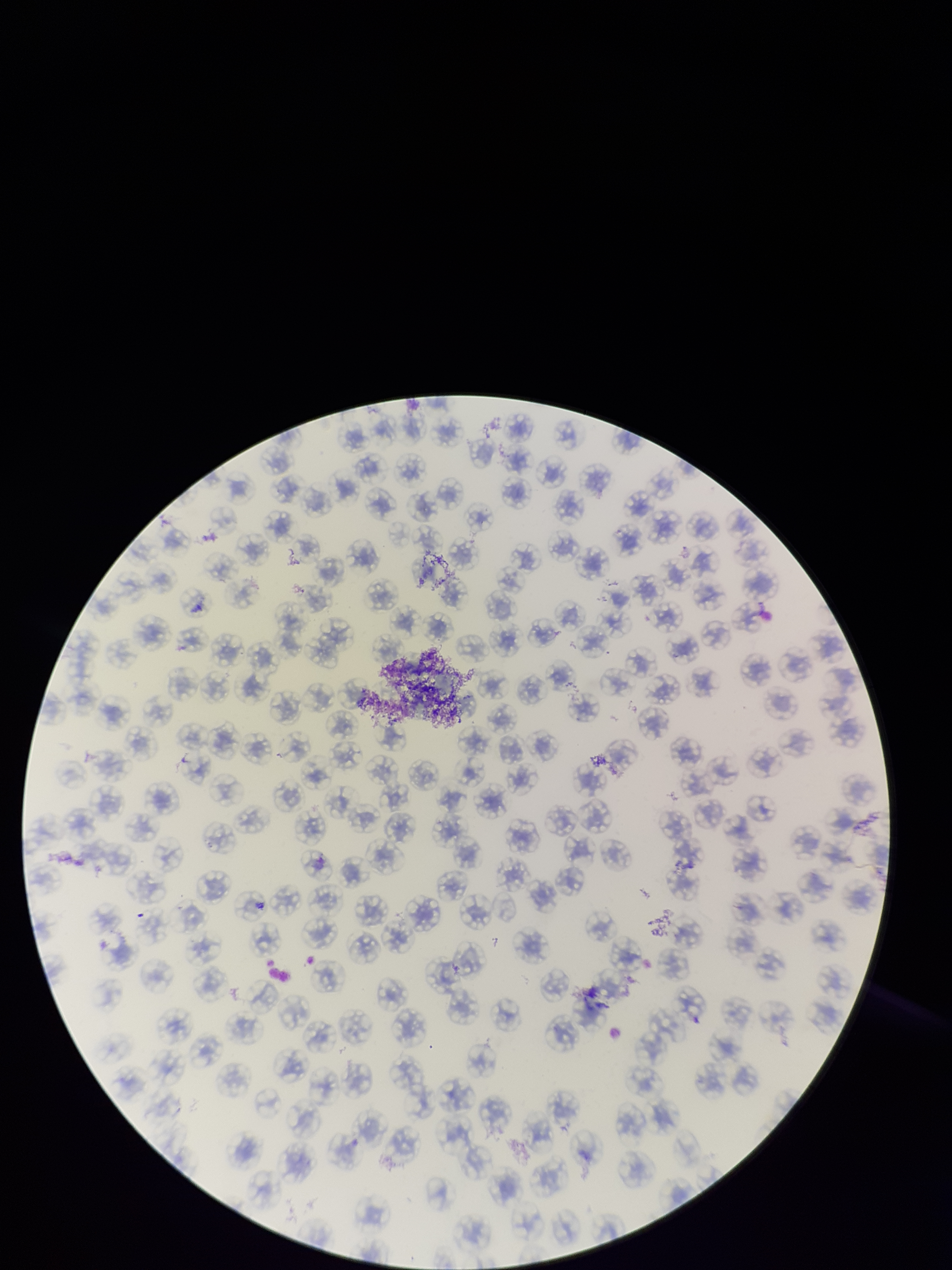

Summary:
  - Capture: smartphone photograph through the microscope eyepiece
  - Field of view: one from this slide
  - Parasitized red blood cells: none detected
  - Red blood cell count: 119
  - Stain: Giemsa
  - Parasitized red blood cell count: 0
  - Preparation: thin
  - Patient malaria status: negative
  - Image size: 952×1270 pixels